State which parasite is depicted.
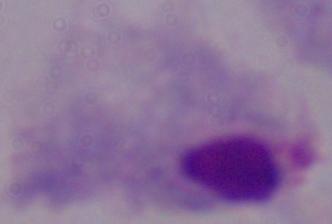
This is a trichomonad.

Summary:
  - Modality: micrograph
  - Magnification: 1000x